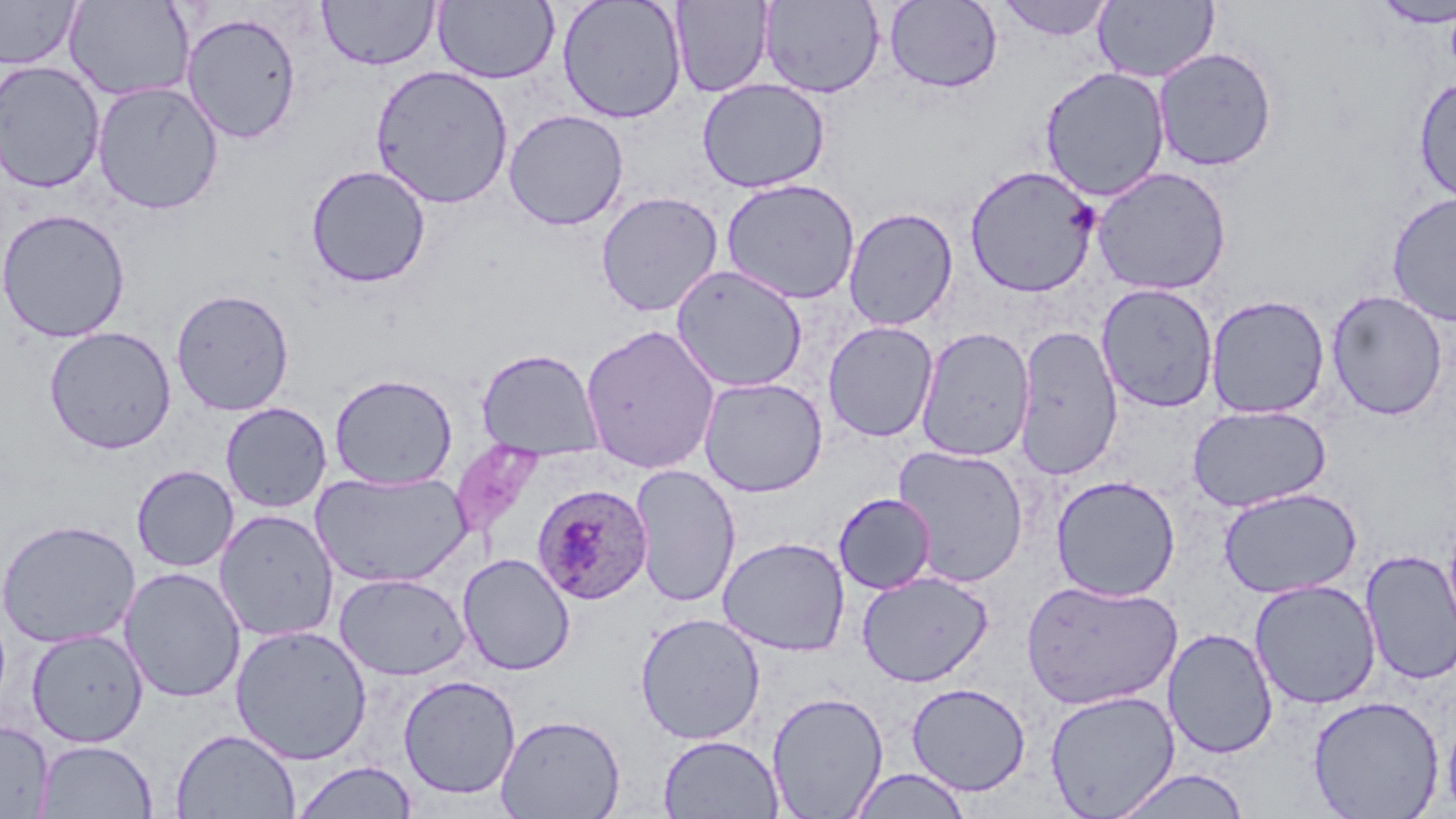

Summary:
  - Coordinate format: approximate bounding boxes as named x1/y1/x2/y2 corners in pixels
  - Plasmodium ovale-infected red blood cell locations: (x1=531, y1=483, x2=653, y2=606)
  - Uninfected red blood cell locations: (x1=0, y1=0, x2=81, y2=69), (x1=63, y1=0, x2=194, y2=102), (x1=317, y1=0, x2=439, y2=70), (x1=433, y1=0, x2=559, y2=84), (x1=556, y1=0, x2=687, y2=123), (x1=995, y1=0, x2=1115, y2=41), (x1=670, y1=1, x2=773, y2=97), (x1=759, y1=1, x2=885, y2=98), (x1=884, y1=1, x2=1003, y2=93), (x1=1093, y1=1, x2=1220, y2=83), (x1=1372, y1=1, x2=1456, y2=28), (x1=181, y1=11, x2=303, y2=144), (x1=1153, y1=47, x2=1278, y2=172), (x1=0, y1=60, x2=106, y2=193), (x1=370, y1=64, x2=514, y2=209), (x1=1039, y1=66, x2=1170, y2=202), (x1=1412, y1=75, x2=1456, y2=203), (x1=697, y1=78, x2=830, y2=194), (x1=91, y1=80, x2=225, y2=216), (x1=503, y1=109, x2=629, y2=231), (x1=305, y1=164, x2=431, y2=288), (x1=964, y1=165, x2=1101, y2=298), (x1=1092, y1=167, x2=1232, y2=295), (x1=720, y1=178, x2=861, y2=304), (x1=595, y1=191, x2=724, y2=317), (x1=1386, y1=192, x2=1456, y2=326), (x1=843, y1=207, x2=959, y2=331), (x1=0, y1=208, x2=131, y2=343), (x1=670, y1=264, x2=808, y2=393), (x1=1096, y1=283, x2=1219, y2=413), (x1=171, y1=288, x2=294, y2=416), (x1=1326, y1=290, x2=1449, y2=421), (x1=1205, y1=294, x2=1331, y2=419), (x1=823, y1=321, x2=939, y2=442), (x1=581, y1=323, x2=722, y2=474), (x1=1013, y1=324, x2=1124, y2=481), (x1=43, y1=325, x2=177, y2=455), (x1=915, y1=326, x2=1036, y2=462), (x1=475, y1=349, x2=604, y2=461), (x1=329, y1=373, x2=458, y2=490), (x1=698, y1=377, x2=828, y2=497), (x1=220, y1=402, x2=332, y2=513), (x1=1187, y1=404, x2=1332, y2=512), (x1=892, y1=444, x2=1030, y2=588), (x1=131, y1=464, x2=239, y2=572), (x1=629, y1=464, x2=741, y2=608), (x1=311, y1=469, x2=473, y2=588), (x1=1050, y1=475, x2=1181, y2=601), (x1=1218, y1=487, x2=1361, y2=599), (x1=833, y1=493, x2=936, y2=594), (x1=213, y1=508, x2=339, y2=642), (x1=0, y1=518, x2=141, y2=649), (x1=717, y1=536, x2=850, y2=656), (x1=1360, y1=550, x2=1456, y2=685), (x1=457, y1=553, x2=576, y2=676), (x1=119, y1=566, x2=246, y2=703), (x1=857, y1=570, x2=993, y2=687), (x1=334, y1=573, x2=470, y2=680), (x1=1021, y1=578, x2=1183, y2=710), (x1=1249, y1=579, x2=1381, y2=709), (x1=635, y1=612, x2=766, y2=745), (x1=230, y1=623, x2=373, y2=765), (x1=1162, y1=627, x2=1279, y2=759), (x1=26, y1=628, x2=149, y2=747), (x1=397, y1=675, x2=521, y2=800), (x1=906, y1=682, x2=1031, y2=796), (x1=1044, y1=689, x2=1180, y2=818), (x1=766, y1=690, x2=888, y2=818), (x1=1308, y1=694, x2=1444, y2=819), (x1=1441, y1=704, x2=1456, y2=815), (x1=494, y1=712, x2=626, y2=818), (x1=0, y1=720, x2=54, y2=818), (x1=171, y1=727, x2=301, y2=818), (x1=658, y1=734, x2=784, y2=818), (x1=36, y1=740, x2=158, y2=818), (x1=290, y1=760, x2=419, y2=818), (x1=847, y1=768, x2=972, y2=818), (x1=1109, y1=768, x2=1251, y2=819)
  - Slide-level diagnosis: Plasmodium ovale
  - Preparation: thin blood film
  - Modality: optical microscopy
  - Image size: 1456×819 pixels
  - Field of view: single
  - Magnification: 1000x
  - Stain: May-Grünwald-Giemsa